Name the malaria species.
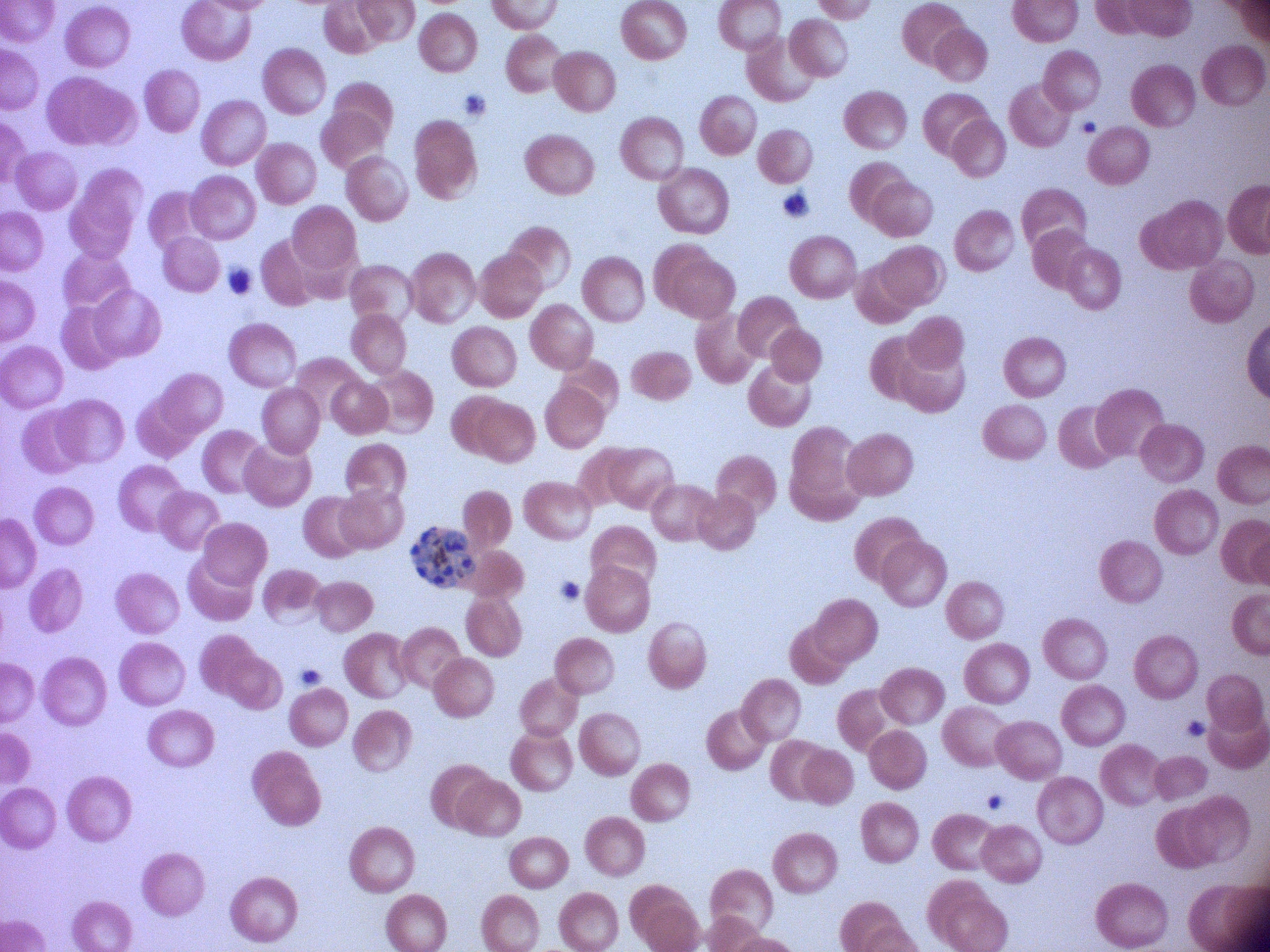

Plasmodium falciparum.

Approximate bounding boxes as (x1, y1, x2, y2) in pixels, from the source annotation, which is not necessarily exhaustive.
Summary:
  - Schizont locations: (410, 527, 476, 589)
  - Microscope: Leica DM2000 with built-in camera
  - Field of view: one from this slide
  - Stain: Giemsa
  - Preparation: thin blood smear
  - Image size: 1270×952 pixels
  - Magnification: 100x